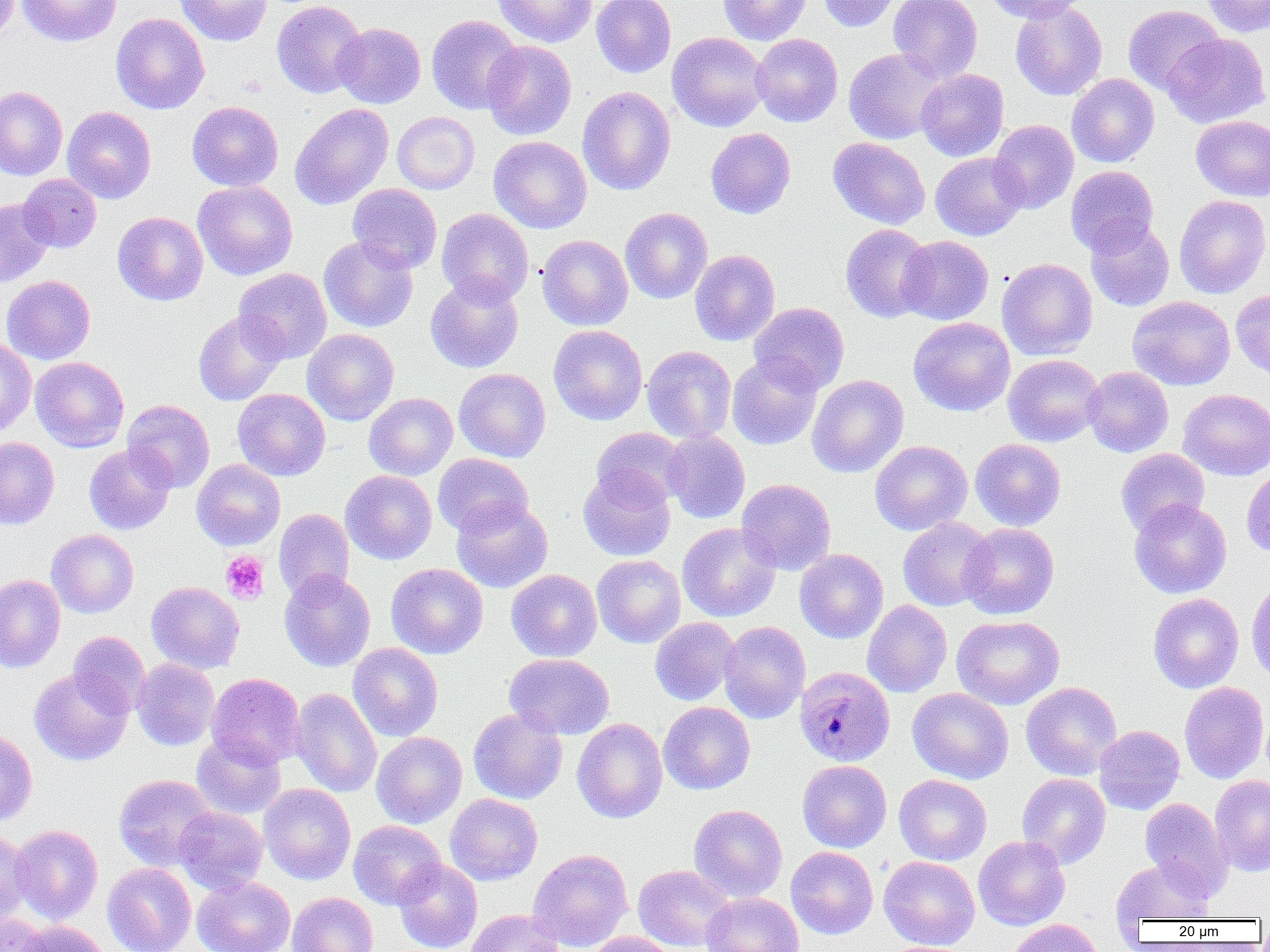 Approximate bounding boxes as (x1,y1)-(x2,y2) corner pairs in pixels. Plasmodium malariae-infected red blood cell locations: (794,666)-(895,767). Platelet locations: (220,551)-(270,604). Uninfected red blood cell locations: (0,0)-(20,41), (17,0)-(121,46), (175,0)-(272,46), (271,0)-(368,98), (491,0)-(596,47), (591,0)-(676,78), (718,0)-(811,45), (818,0)-(902,32), (888,0)-(982,82), (983,0)-(1090,23), (1201,0)-(1270,37), (1010,1)-(1108,101), (1123,5)-(1224,95), (110,13)-(210,114), (426,15)-(524,114), (334,22)-(426,108), (667,32)-(769,132), (1162,32)-(1270,128), (751,33)-(843,127), (481,40)-(576,140), (843,48)-(945,144), (915,68)-(1009,162), (1067,74)-(1159,167), (0,86)-(68,181), (577,86)-(676,196), (186,101)-(283,191), (290,103)-(393,209), (62,106)-(156,204), (392,111)-(479,194), (1191,115)-(1270,202), (989,120)-(1079,214), (705,128)-(795,218), (488,136)-(592,233), (828,137)-(930,229), (930,152)-(1028,241), (1065,165)-(1159,256), (18,174)-(102,252), (193,180)-(297,280), (347,183)-(442,273), (1174,195)-(1270,298), (0,199)-(55,289), (620,207)-(713,304), (436,208)-(534,305), (112,212)-(208,305), (1086,221)-(1174,311), (840,224)-(934,323), (537,234)-(633,331), (897,235)-(994,325), (319,236)-(418,333), (690,250)-(780,346), (996,258)-(1098,360), (234,268)-(332,363), (425,274)-(524,373), (1,275)-(95,365), (1231,289)-(1270,379), (1128,296)-(1236,390), (749,302)-(849,395), (193,311)-(286,406), (908,317)-(1015,416), (548,325)-(648,425), (302,328)-(399,425), (0,338)-(37,436), (642,346)-(736,444), (727,354)-(822,450), (1004,354)-(1105,447), (30,356)-(129,452), (1083,366)-(1173,457), (453,368)-(550,462), (807,374)-(908,478), (233,389)-(330,481), (1178,389)-(1270,480), (364,393)-(457,480), (122,399)-(215,492), (591,427)-(689,507), (662,429)-(750,524), (0,437)-(59,529), (970,438)-(1066,531), (869,440)-(972,535), (84,444)-(176,535), (1115,448)-(1210,536), (432,453)-(534,538), (192,459)-(285,551), (578,466)-(676,562), (340,470)-(437,564), (736,478)-(836,575), (451,498)-(553,593), (1129,498)-(1232,599), (274,509)-(354,600), (897,517)-(996,611), (677,522)-(780,622), (959,522)-(1059,619), (46,529)-(139,618), (794,549)-(888,643), (591,555)-(686,648), (386,563)-(488,659), (279,569)-(376,671), (506,569)-(602,662), (0,574)-(65,673), (1246,578)-(1270,686), (146,581)-(244,673), (1148,593)-(1244,693), (862,600)-(952,697), (952,615)-(1064,709), (649,617)-(739,706), (719,621)-(810,724), (67,631)-(151,717), (348,642)-(443,741), (503,653)-(614,739), (132,658)-(219,750), (28,668)-(133,766), (206,672)-(306,768), (1021,681)-(1122,780), (1178,681)-(1269,783), (291,687)-(382,798), (907,688)-(1014,784), (658,701)-(755,794), (468,709)-(568,804), (572,718)-(667,823), (1094,725)-(1185,815), (0,729)-(37,825), (191,732)-(286,819), (371,732)-(467,828), (797,760)-(892,852), (1017,772)-(1111,868), (114,774)-(217,871), (894,774)-(992,865), (1210,774)-(1270,876), (259,783)-(356,884), (445,793)-(542,885), (1140,798)-(1232,897), (688,803)-(787,902), (174,806)-(268,894), (348,819)-(446,910), (10,824)-(103,924), (0,827)-(33,927), (973,835)-(1070,930), (785,846)-(878,939), (528,848)-(634,951), (879,855)-(980,951), (394,858)-(483,952), (1112,858)-(1215,924), (102,862)-(196,952), (632,864)-(736,951), (192,875)-(295,952), (287,892)-(378,952), (701,892)-(804,952), (464,908)-(565,952), (0,913)-(49,952), (1006,919)-(1104,952), (15,921)-(109,952), (583,932)-(680,952). Slide-level diagnosis: Plasmodium malariae. Optical microscopy. Thin blood smear. 1000x magnification. One field of a larger specimen. Image is 1270×952 pixels.